Draw a bounding box around every malaria parasite.
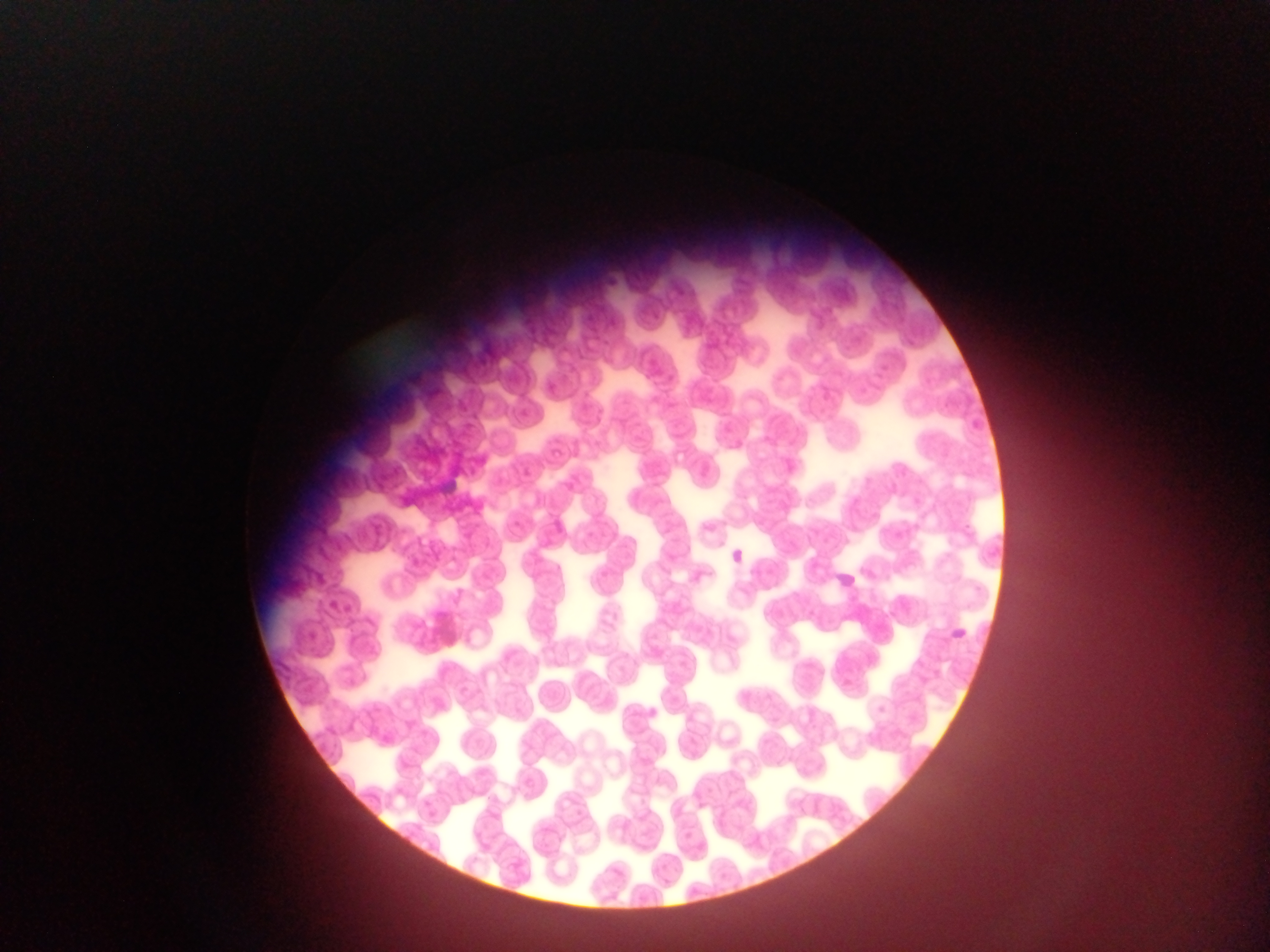

Approximate bounding boxes as left top right bottom in pixels.
Malaria parasites: 511 517 520 525; 724 544 769 576; 831 569 872 594; 949 624 970 643.

Summary:
  - Country: Ghana
  - Image size: 1270×952 pixels
  - Field of view: single
  - Preparation: thin blood smear
  - Capture: mobile-phone photograph through a microscope